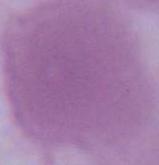

Captured at 1000x magnification. An erythrocyte is seen. Micrograph.